State the preparation type.
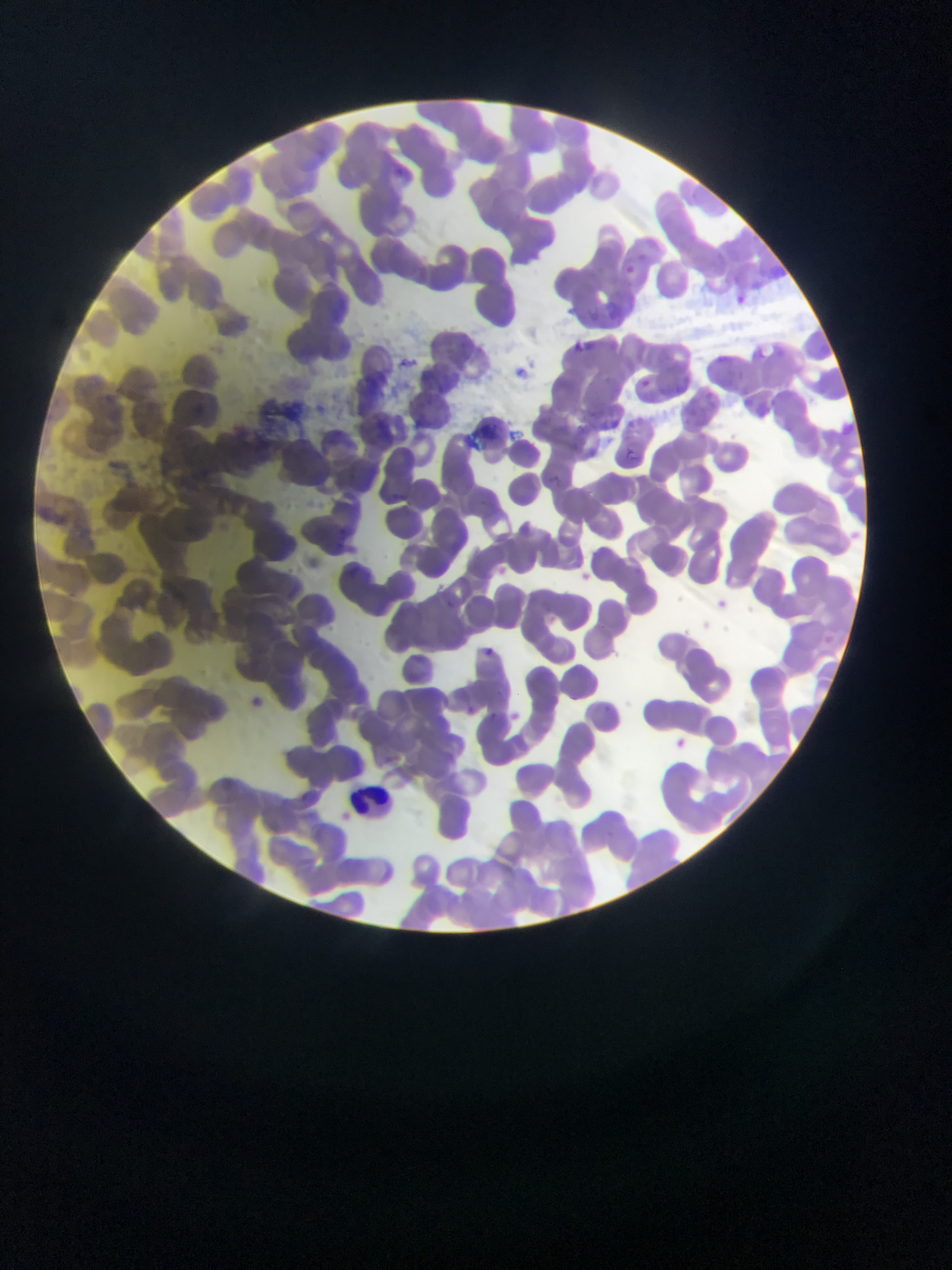

Thin blood film.

Approximate bounding boxes as (left, top, right, bottom) in pixels.
Summary:
  - Leukocyte locations: (346, 784, 393, 820)
  - Country: Ghana
  - Field of view: single
  - Image size: 952×1270 pixels
  - Capture: mobile-phone photograph through a microscope